Outline each Plasmodium ovale-infected red blood cell.
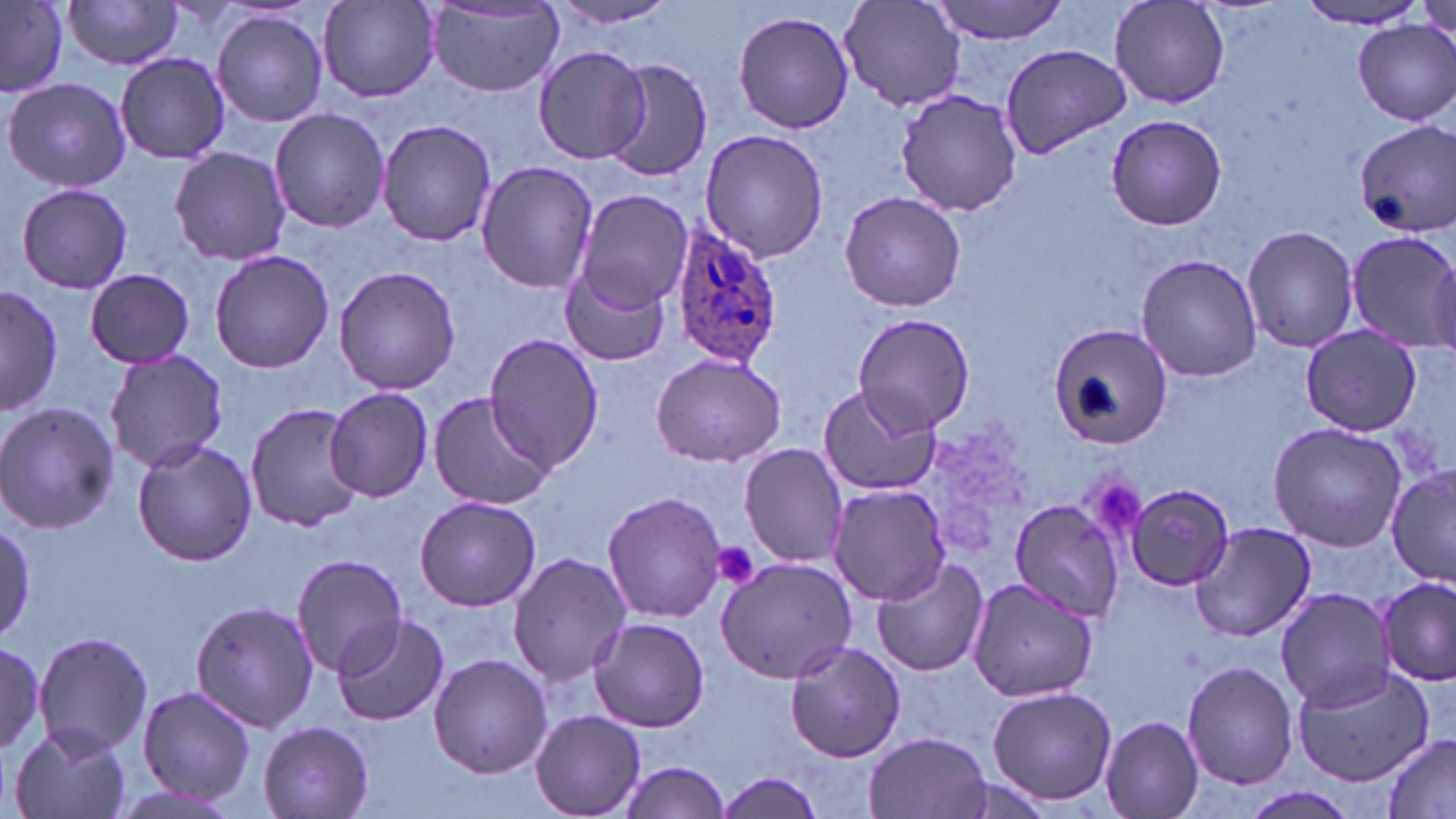

Approximate bounding boxes as (x1,y1)-(x2,y2) corner pairs in pixels.
Plasmodium ovale-infected red blood cells: (668,222)-(783,367).

slide-level diagnosis = Plasmodium ovale
image size = 1456×819 pixels
platelet locations = approximate bounding boxes as (x1,y1)-(x2,y2) corner pairs in pixels: (1095,482)-(1145,536), (713,542)-(761,589)
preparation = thin blood smear
magnification = 1000x
stain = May-Grünwald-Giemsa
uninfected red blood cell locations = approximate bounding boxes as (x1,y1)-(x2,y2) corner pairs in pixels: (928,0)-(1070,43), (1108,0)-(1232,111), (1298,0)-(1433,30), (63,1)-(186,71), (547,1)-(681,28), (0,2)-(68,97), (319,2)-(441,101), (837,2)-(967,111), (424,6)-(566,95), (732,9)-(855,135), (211,10)-(330,127), (1350,19)-(1456,126), (997,43)-(1131,159), (535,45)-(652,165), (114,52)-(229,165), (604,57)-(713,183), (4,76)-(132,193), (894,86)-(1024,217), (268,107)-(391,233), (1105,113)-(1227,231), (375,118)-(500,247), (1353,120)-(1456,236), (700,129)-(829,263), (170,146)-(294,267), (474,161)-(598,293), (16,183)-(134,294), (571,188)-(694,315), (840,190)-(965,313), (1241,223)-(1358,354), (1344,229)-(1456,349), (208,249)-(336,372), (1136,254)-(1262,382), (333,265)-(462,395), (560,267)-(669,368), (85,269)-(195,368), (1,285)-(60,416), (849,313)-(975,440), (1047,319)-(1172,451), (1300,328)-(1423,435), (484,334)-(606,474), (105,349)-(227,472), (650,353)-(786,466), (816,385)-(941,498), (325,388)-(433,501), (428,391)-(552,510), (0,400)-(119,535), (245,402)-(367,533), (1267,422)-(1407,552), (131,439)-(258,568), (739,443)-(848,567), (1387,467)-(1456,585), (1126,482)-(1235,591), (829,484)-(953,606), (601,490)-(727,623), (415,496)-(543,611), (1011,497)-(1128,619), (0,516)-(36,641), (1189,522)-(1315,642), (507,551)-(631,685), (289,553)-(408,678), (715,556)-(858,683), (870,556)-(988,676), (965,577)-(1100,702), (1376,578)-(1454,686), (1275,587)-(1394,708), (190,600)-(320,732), (331,612)-(450,727), (589,615)-(710,732), (34,631)-(156,757), (0,639)-(54,759), (784,640)-(906,763), (428,653)-(552,778), (1183,660)-(1298,790), (1290,665)-(1435,786), (136,686)-(257,803), (986,686)-(1118,807), (531,709)-(646,818), (1100,715)-(1207,819), (258,721)-(375,819), (9,726)-(132,819), (863,732)-(992,819), (1381,732)-(1456,819), (617,760)-(732,818), (712,770)-(828,818)
modality = light microscopy
field of view = one of a larger specimen